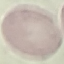
Result: no malaria parasites detected. Giemsa-stained preparation. Cell patch, automatically extracted from a larger field of view and resized to 64 × 64 pixels. Thin blood smear. Photographed with a smartphone camera at the microscope eyepiece.